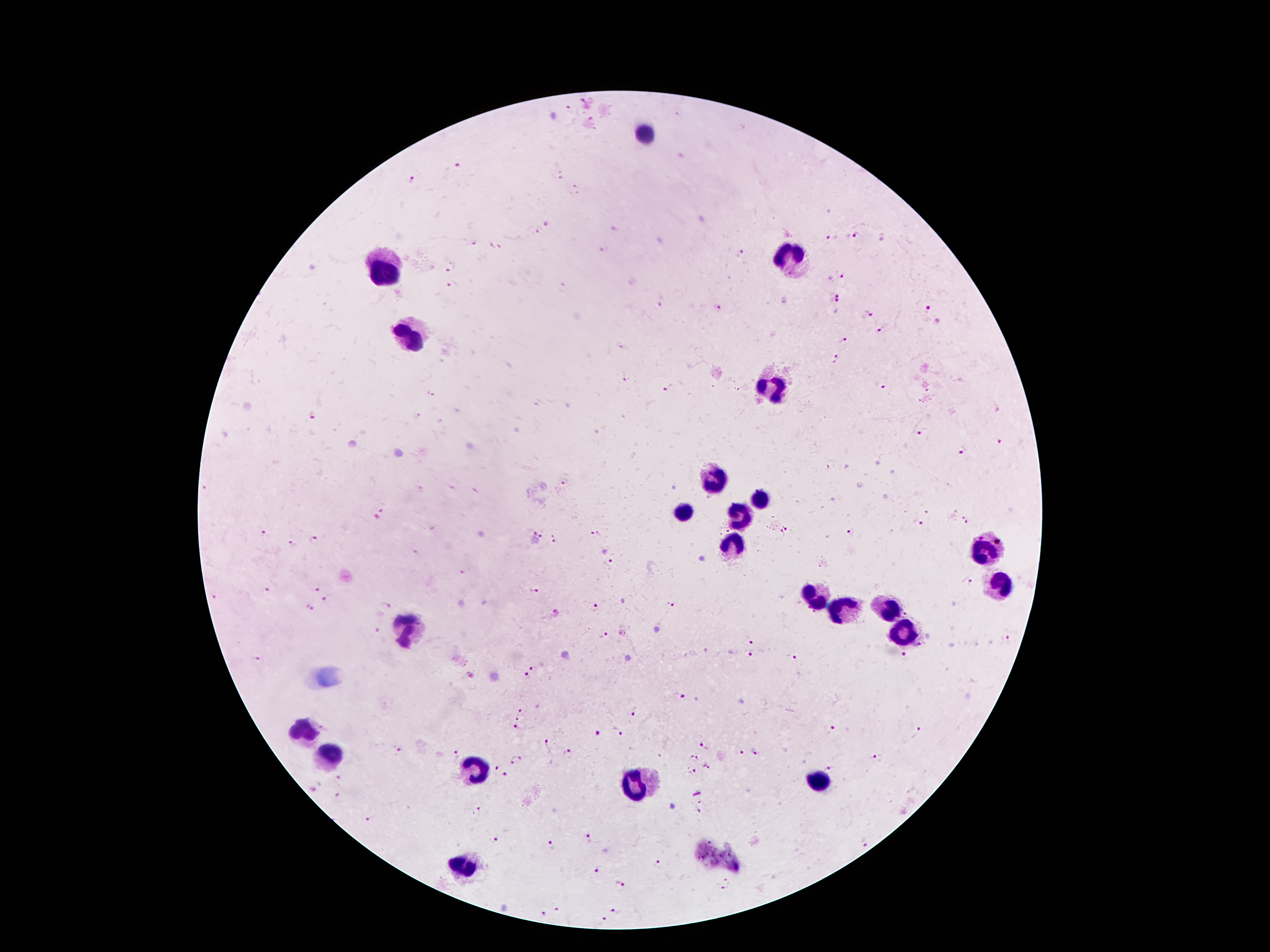

{
  "field_of_view": "single",
  "stain": "Giemsa",
  "capture": "smartphone camera through the microscope eyepiece",
  "image_size": "1270×952 pixels",
  "leukocyte_locations": "approximate centers as {x, y} in pixels: {643, 134}, {793, 255}, {385, 268}, {410, 339}, {769, 390}, {715, 483}, {759, 503}, {685, 514}, {738, 516}, {732, 542}, {984, 549}, {1005, 586}, {818, 595}, {887, 611}, {835, 612}, {406, 633}, {902, 635}, {299, 729}, {333, 752}, {473, 767}, {818, 779}, {637, 785}, {463, 863}",
  "magnification": "100x",
  "patient_malaria_status": "positive for Plasmodium falciparum",
  "preparation": "thick blood smear",
  "plasmodium_parasite_locations": "approximate centers as {x, y} in pixels: {567, 108}, {590, 119}, {458, 166}, {560, 176}, {414, 180}, {573, 184}, {578, 194}, {547, 224}, {613, 229}, {537, 233}, {858, 235}, {830, 238}, {475, 244}, {496, 247}, {602, 250}, {743, 252}, {451, 269}, {842, 276}, {451, 285}, {836, 299}, {661, 303}, {718, 307}, {928, 308}, {870, 313}, {878, 329}, {844, 339}, {619, 347}, {835, 357}, {626, 378}, {881, 386}, {668, 390}, {433, 394}, {312, 415}, {924, 434}, {999, 441}, {963, 451}, {565, 483}, {421, 489}, {381, 513}, {965, 521}, {921, 525}, {784, 532}, {539, 533}, {595, 534}, {851, 534}, {261, 535}, {316, 539}, {555, 539}, {290, 545}, {416, 553}, {608, 561}, {463, 573}, {967, 581}, {314, 590}, {265, 591}, {535, 591}, {214, 597}, {325, 600}, {386, 606}, {670, 606}, {308, 608}, {595, 608}, {906, 613}, {375, 631}, {606, 635}, {1008, 638}, {749, 640}, {748, 656}, {905, 656}, {791, 658}, {254, 659}, {532, 668}, {523, 676}, {680, 696}, {521, 710}, {635, 710}, {518, 718}, {517, 728}, {830, 730}, {618, 732}, {919, 733}, {597, 734}, {548, 744}, {704, 745}, {398, 750}, {455, 753}, {740, 753}, {568, 754}, {755, 754}, {696, 759}, {875, 759}, {516, 760}, {707, 766}, {495, 768}, {830, 769}, {691, 772}, {505, 775}, {311, 790}, {336, 798}, {702, 806}, {478, 810}, {368, 820}, {588, 837}, {495, 840}, {866, 843}, {552, 846}, {658, 864}, {597, 870}, {621, 884}, {727, 885}, {556, 910}, {617, 912}, {542, 914}, {603, 921}"
}